Classify this cell by malaria status.
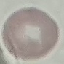
Uninfected.

Cell patch, automatically extracted from a larger field of view and resized to 64 × 64 pixels. Thin blood smear. Giemsa-stained preparation. Photographed with a smartphone camera at the microscope eyepiece.